State which parasite is depicted.
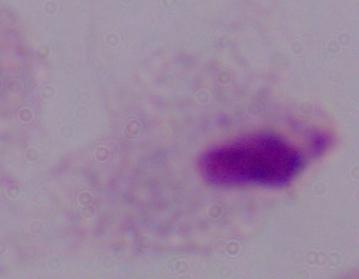
This is a trichomonad.

1000x magnification. Photomicrograph.